State which cell type is depicted.
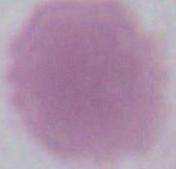
This is an erythrocyte.

Summary:
  - Magnification: 1000x
  - Modality: photomicrograph